Locate platelets.
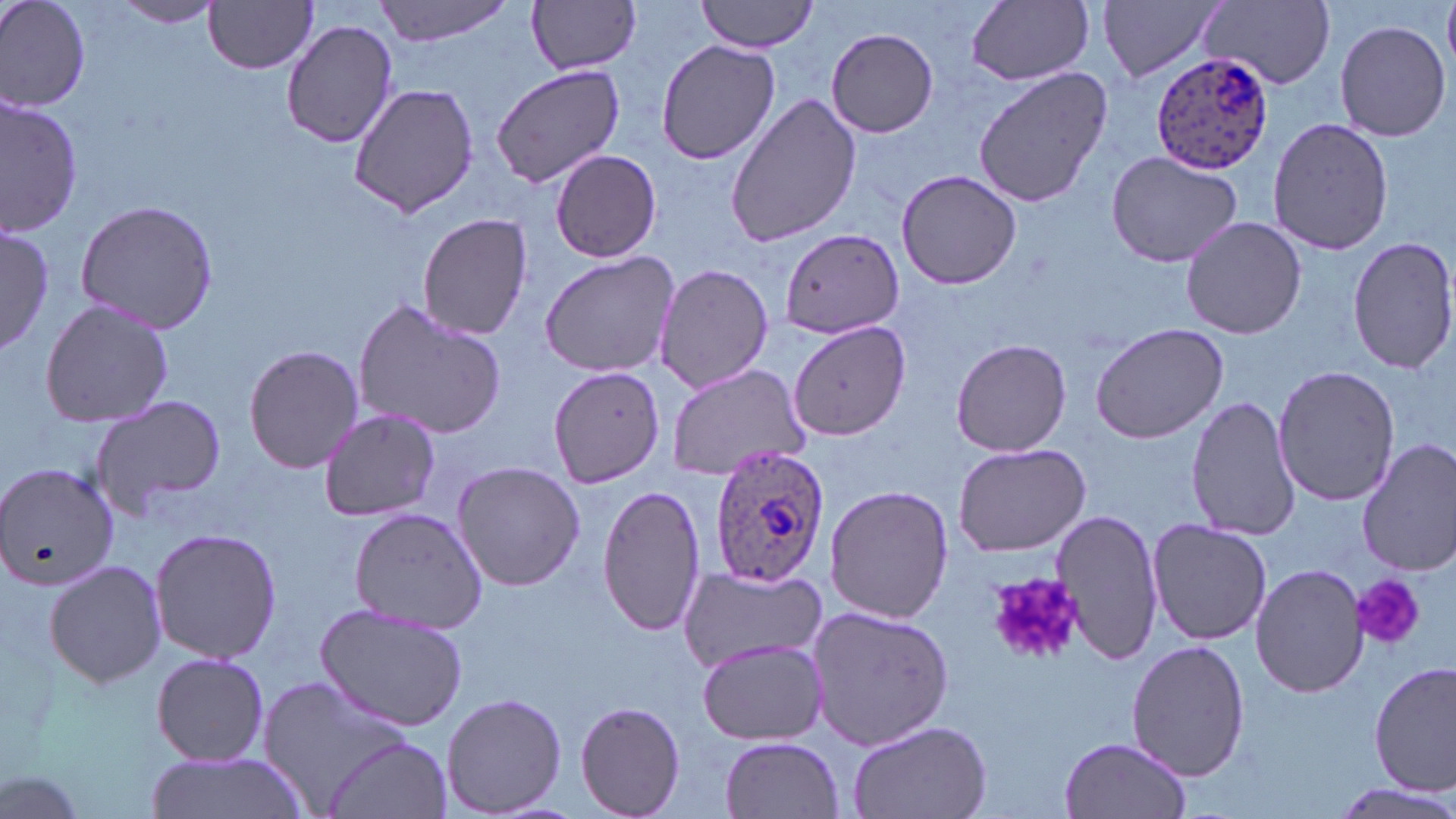
Approximate bounding boxes as [x1, y1, x2, y2] in pixels.
Platelets: [985, 569, 1081, 668], [1350, 574, 1424, 650].

Plasmodium ovale-infected red blood cell locations: [1150, 49, 1274, 173], [708, 445, 829, 588]. Uninfected red blood cell locations: [0, 0, 91, 111], [372, 0, 517, 46], [697, 0, 819, 54], [1098, 0, 1227, 85], [1199, 0, 1336, 90], [114, 1, 225, 28], [526, 1, 642, 75], [965, 1, 1096, 86], [203, 2, 320, 74], [281, 20, 400, 148], [1334, 20, 1451, 141], [829, 26, 940, 137], [653, 40, 779, 165], [490, 64, 628, 189], [973, 66, 1110, 208], [348, 83, 481, 216], [724, 92, 862, 246], [1, 93, 84, 236], [1267, 116, 1394, 257], [550, 148, 663, 263], [1105, 149, 1245, 270], [896, 168, 1023, 290], [74, 198, 221, 334], [418, 211, 536, 340], [1182, 216, 1307, 339], [0, 224, 52, 355], [778, 231, 905, 338], [1347, 236, 1455, 376], [538, 249, 683, 378], [655, 263, 774, 395], [38, 297, 174, 430], [351, 298, 509, 442], [1088, 319, 1232, 445], [790, 320, 912, 441], [951, 337, 1072, 457], [243, 343, 364, 473], [665, 361, 811, 482], [1273, 365, 1398, 506], [550, 366, 664, 488], [87, 395, 228, 520], [1187, 395, 1303, 542], [316, 409, 442, 522], [1356, 436, 1456, 576], [952, 442, 1091, 557], [451, 462, 587, 592], [0, 463, 118, 592], [596, 482, 708, 638], [824, 484, 954, 624], [348, 507, 488, 633], [1054, 507, 1165, 666], [1146, 518, 1274, 646], [149, 526, 283, 665], [43, 559, 166, 687], [1251, 562, 1368, 698], [677, 567, 829, 672], [314, 604, 469, 731], [806, 605, 954, 752], [697, 638, 827, 745], [1127, 641, 1250, 781], [149, 651, 271, 767], [1370, 661, 1455, 796], [258, 677, 415, 812], [440, 692, 568, 817], [572, 701, 688, 818], [843, 717, 991, 819], [323, 734, 452, 819], [720, 735, 845, 817], [1058, 735, 1193, 819], [147, 751, 312, 819], [1, 766, 91, 819], [1327, 781, 1456, 817]. Slide-level diagnosis: Plasmodium ovale. May-Grünwald-Giemsa stain. Optical microscopy. Image is 1456×819 pixels. Thin blood smear. One field of a larger specimen. 1000x magnification.